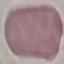 Malaria status: uninfected. Thin blood smear. Giemsa stain. Cell patch, automatically extracted from a larger field of view and resized to 64 × 64 pixels. Photographed with a smartphone camera at the microscope eyepiece.